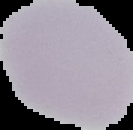

image_size: 133×130 pixels
result: negative for Plasmodium parasites
preparation: thin blood smear
image_type: segmented cell region with the area outside set to black